Identify the cell.
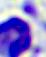

A leukocyte.

modality: photomicrograph
magnification: 400x